Assess the morphology of the erythrocytes.
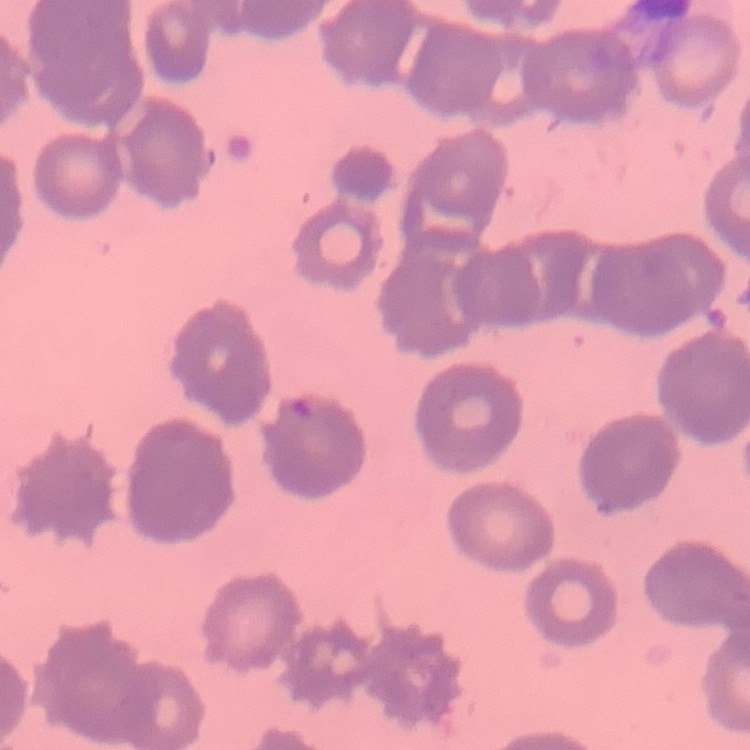

Rouleaux formation.

Thin blood film. Field's or Giemsa stain. Square crop of a larger photomicrograph.